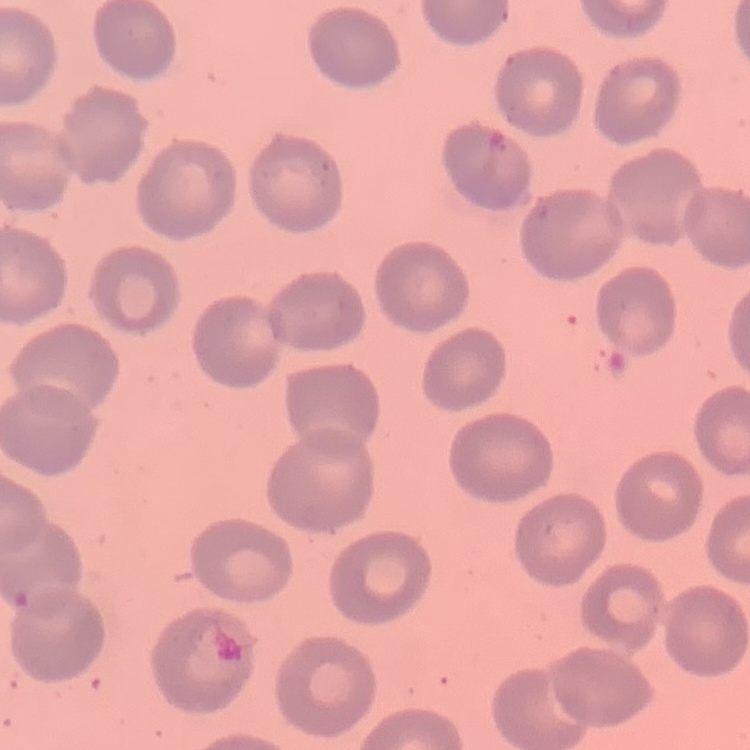

The erythrocytes show no rouleaux formation. Stained with either Field's or Giemsa. Thin blood film. Square crop of a larger photomicrograph.